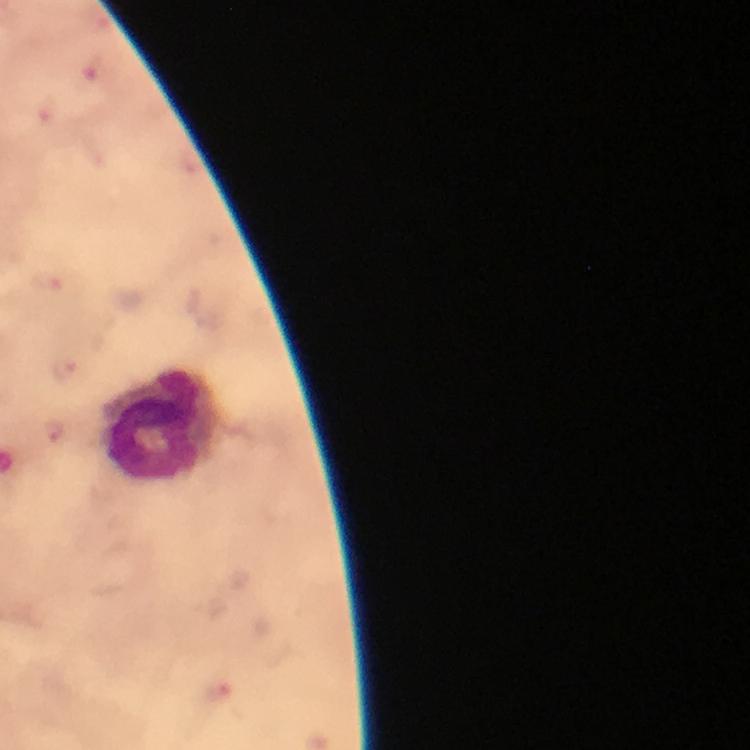
Approximate centers as (x, y) in pixels. Malaria parasite locations: (94, 66), (47, 113), (45, 282), (63, 368), (52, 433), (216, 688). Leukocyte locations: (158, 425). Smartphone photograph taken through a microscope. From a malaria diagnostic workup. 100x magnification. A crop from one field of view. Image is 750×750 pixels. Thick blood smear. Giemsa stain. Immersion oil was used.